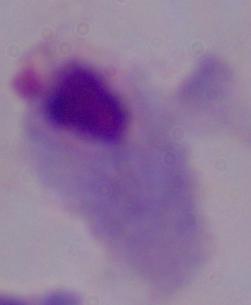
identification: trichomonad
modality: micrograph
magnification: 1000x